Evaluate for Plasmodium parasites.
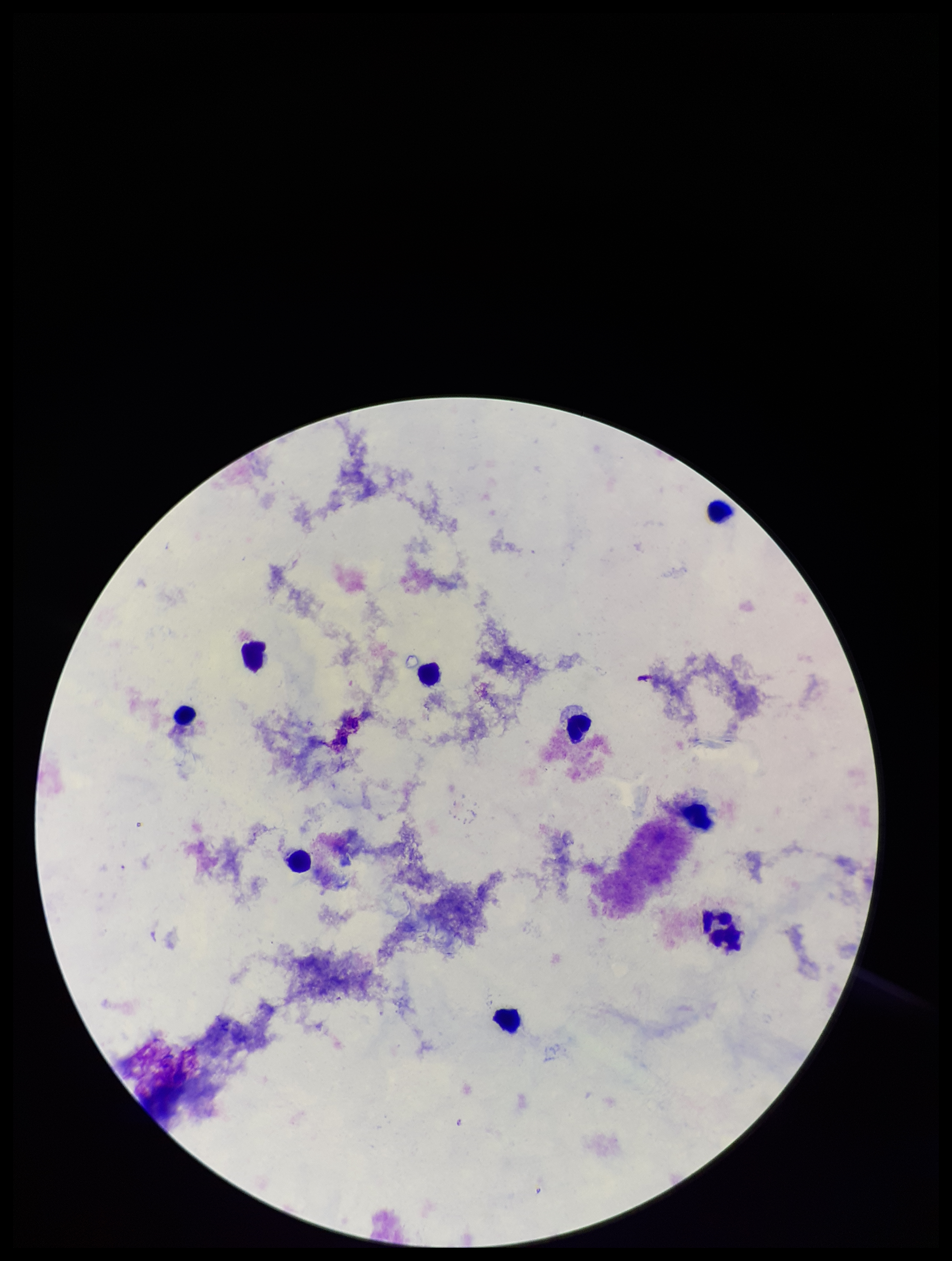

None seen.

Summary:
  - Parasite count: 0
  - Patient malaria status: negative
  - Leukocyte count: 9
  - Preparation: thick smear
  - Capture: smartphone photograph through the microscope eyepiece
  - Image size: 952×1261 pixels
  - Field of view: single
  - Stain: Giemsa